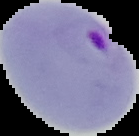
image size = 139×136 pixels
image type = segmented cell region with the area outside set to black
preparation = thin blood smear
result = malaria parasites identified